State which cell type is depicted.
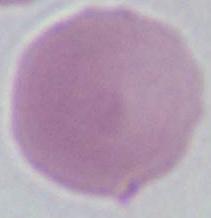
This is an erythrocyte.

Photomicrograph. Captured at 1000x magnification.